Report the malaria status of this cell.
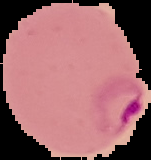
It is parasitized.

From a thin blood film. Image is 151×160 pixels. The area outside the segmented cell region is set to black.